Describe the morphology of the erythrocytes.
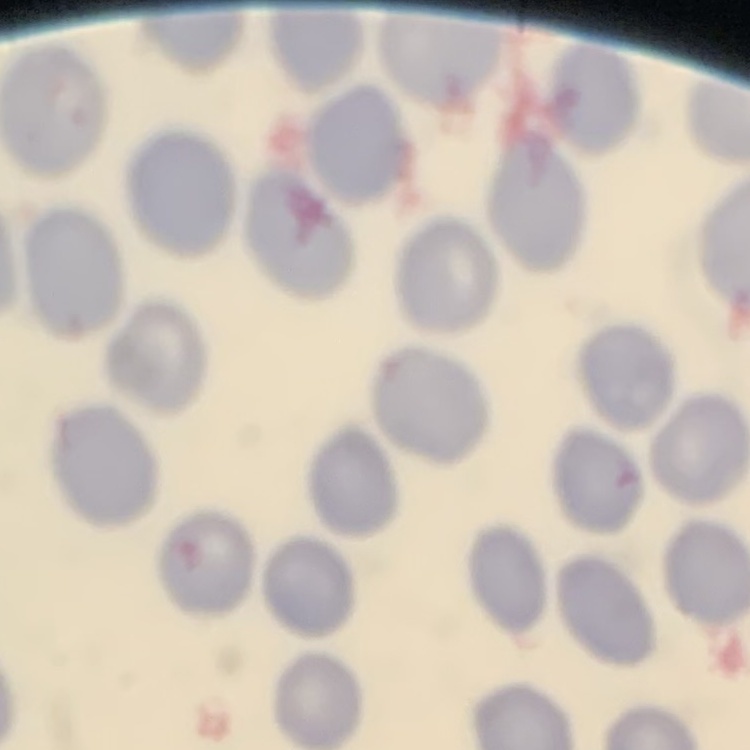

They show no rouleaux formation.

Stained with either Field's or Giemsa. One tile cut from a larger photomicrograph. Thin blood film.